Locate every blood parasite and identify its species.
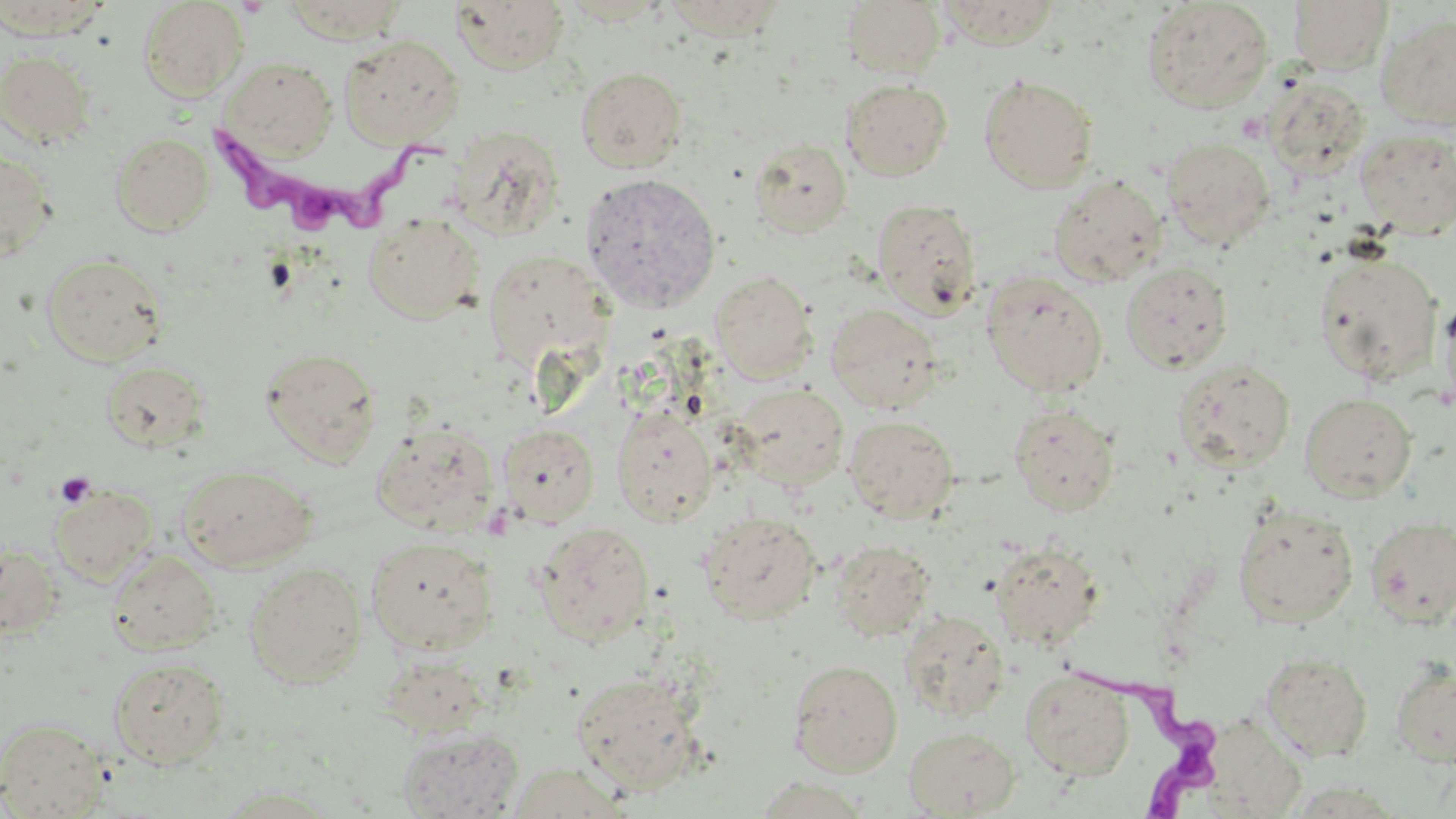
Approximate bounding boxes as (x1,y1)-(x2,y2) corner pairs in pixels.
Trypanosoma brucei: (198,124)-(456,247), (1060,660)-(1219,819).
No Plasmodium falciparum, Plasmodium ovale, Plasmodium malariae, Plasmodium vivax, or Babesia divergens observed.

Platelet locations: (54,472)-(96,509). Uninfected red blood cell locations: (0,0)-(114,40), (282,0)-(410,43), (662,0)-(791,40), (934,0)-(1065,48), (137,1)-(248,102), (450,1)-(571,74), (841,1)-(947,77), (1142,1)-(1273,112), (1288,1)-(1392,74), (1376,11)-(1456,131), (338,34)-(464,148), (0,51)-(96,147), (222,58)-(337,159), (575,66)-(687,172), (979,75)-(1099,193), (1264,78)-(1371,178), (842,79)-(952,181), (1355,128)-(1455,238), (111,132)-(214,236), (1162,137)-(1276,249), (749,138)-(852,238), (0,148)-(58,262), (579,172)-(721,314), (1048,174)-(1167,287), (872,197)-(982,317), (363,213)-(484,323), (484,248)-(615,371), (1313,251)-(1443,384), (40,253)-(167,365), (1121,262)-(1233,373), (710,271)-(817,382), (981,271)-(1108,397), (1437,292)-(1456,415), (825,304)-(944,414), (261,347)-(382,463), (100,359)-(211,452), (1173,359)-(1295,472), (731,383)-(849,491), (1300,392)-(1417,502), (1009,403)-(1121,516), (611,406)-(718,524), (844,416)-(959,523), (371,419)-(498,534), (498,423)-(599,527), (178,463)-(317,571), (49,484)-(157,585), (1232,504)-(1359,627), (699,512)-(822,624), (1365,515)-(1456,629), (533,522)-(655,645), (365,536)-(499,654), (831,540)-(936,641), (989,540)-(1106,651), (0,542)-(64,638), (106,549)-(221,655), (243,562)-(367,688), (898,610)-(1009,722), (377,650)-(490,739), (1259,650)-(1373,762), (108,657)-(229,768), (1391,658)-(1456,767), (788,659)-(903,777), (1021,668)-(1134,781), (570,671)-(704,794), (0,717)-(109,818), (1207,717)-(1308,819), (398,726)-(523,819), (904,726)-(1021,817), (506,763)-(629,818), (749,775)-(872,817), (211,785)-(347,818). Slide-level diagnosis: Trypanosoma brucei. Image is 1456×819 pixels. 1000x magnification. One field of a larger specimen. May-Grünwald-Giemsa-stained preparation. Thin blood film. Optical microscopy.